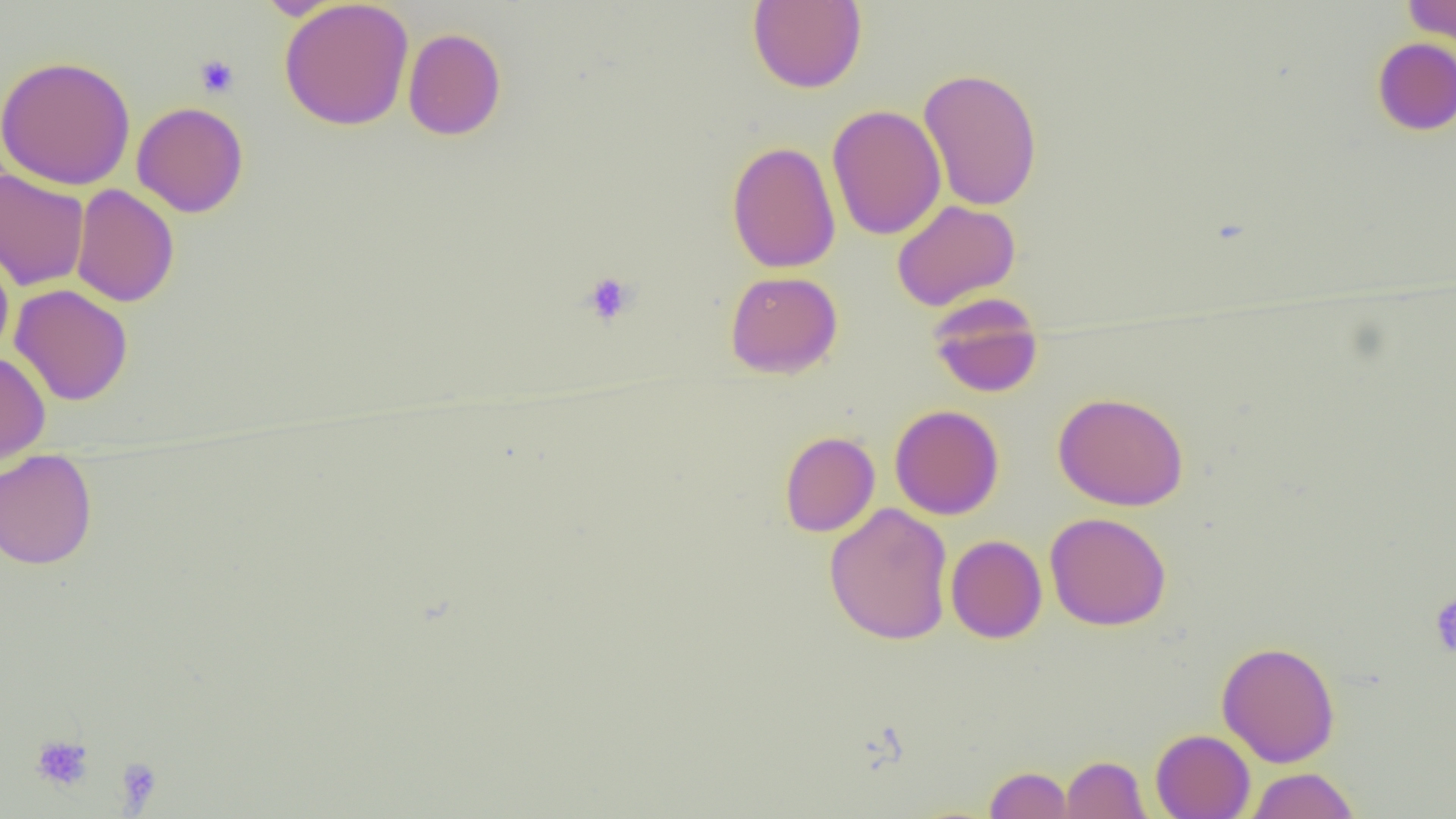 Approximate bounding boxes as (x1, y1, x2, y2) in pixels. Uninfected red blood cell locations: (279, 0, 414, 130), (1404, 0, 1455, 52), (747, 1, 867, 93), (402, 27, 507, 140), (1372, 37, 1456, 136), (0, 55, 136, 190), (918, 67, 1043, 211), (131, 101, 249, 217), (826, 104, 946, 241), (727, 140, 841, 274), (0, 169, 90, 291), (71, 184, 179, 308), (891, 199, 1021, 311), (0, 243, 14, 361), (725, 271, 843, 379), (9, 284, 133, 405), (928, 293, 1044, 398), (0, 351, 51, 466), (1052, 391, 1189, 511), (890, 405, 1004, 520), (779, 431, 880, 537), (0, 449, 98, 570), (824, 503, 954, 646), (1045, 512, 1171, 630), (945, 535, 1047, 644), (1216, 641, 1341, 767), (1150, 729, 1255, 818), (1060, 755, 1151, 818), (984, 765, 1073, 819), (1245, 767, 1360, 819). Platelet locations: (195, 54, 239, 98), (581, 272, 638, 325), (1429, 595, 1456, 657), (30, 733, 95, 792), (114, 757, 163, 811). Slide-level diagnosis: negative for blood parasites. Image is 1456×819 pixels. Optical microscopy. Captured at 1000x magnification. Single field of view. Thin blood film.